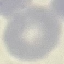

Summary:
  - Malaria status: uninfected
  - Capture: smartphone through the microscope eyepiece
  - Stain: Giemsa
  - Image type: cell patch, automatically extracted from a larger field of view and resized to 64 × 64 pixels
  - Preparation: thin blood film